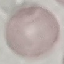
result = no malaria parasites seen
image type = cell patch, automatically extracted from a larger field of view and resized to 64 × 64 pixels
capture = smartphone camera at the microscope eyepiece
preparation = thin blood film
stain = Giemsa